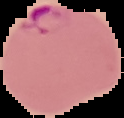 Malaria status: parasitized. Image is 124×118 pixels. Segmented cell region on a black background. From a thin blood film.